Assess this cell for malaria.
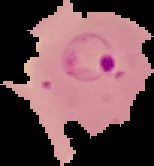

Parasitized.

image_type: cell region segmented out of the field of view; surrounding area masked to black
preparation: thin blood film
image_size: 154×166 pixels